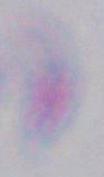

modality: photomicrograph
magnification: 1000x
identification: Toxoplasma gondii